Report the malaria status of this cell.
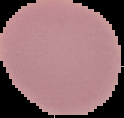

Uninfected.

Image is 124×118 pixels. From a thin blood smear. The area outside the segmented cell region is set to black.